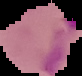

Result: Plasmodium parasites identified. Image is 82×76 pixels. From a thin blood smear. Segmented cell region on a black background.